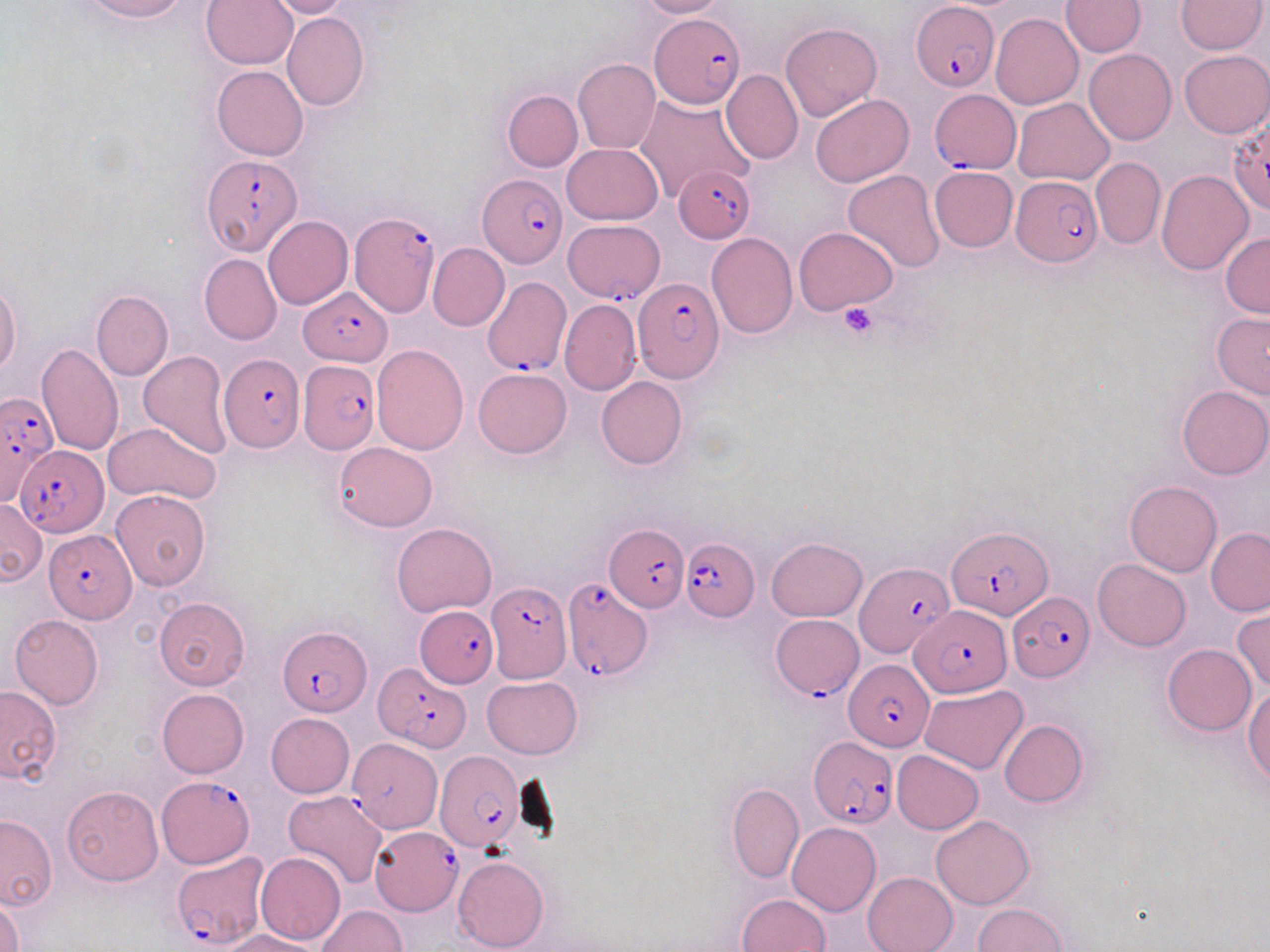
Approximate bounding boxes as (x1, y1, x2, y2) in pixels. Platelet locations: (838, 302, 880, 341). Plasmodium falciparum-infected red blood cell locations: (912, 3, 999, 92), (651, 13, 743, 108), (929, 89, 1021, 172), (1229, 125, 1270, 221), (201, 154, 301, 255), (670, 166, 754, 243), (477, 172, 567, 269), (1012, 174, 1102, 267), (350, 212, 440, 318), (575, 222, 673, 305), (482, 275, 569, 380), (633, 277, 724, 383), (299, 287, 392, 366), (219, 354, 305, 452), (299, 360, 382, 453), (0, 391, 58, 505), (17, 447, 106, 534), (607, 522, 688, 610), (949, 525, 1050, 618), (44, 532, 135, 623), (682, 538, 759, 621), (855, 562, 952, 658), (563, 578, 655, 682), (486, 580, 570, 683), (1010, 591, 1094, 683), (416, 605, 499, 688), (911, 605, 1010, 696), (771, 612, 862, 698), (277, 626, 371, 716), (843, 659, 934, 750), (375, 662, 469, 751), (809, 737, 898, 829), (348, 738, 442, 834), (434, 751, 524, 853), (159, 775, 254, 869), (370, 826, 463, 914), (171, 852, 269, 950). Uninfected red blood cell locations: (79, 0, 188, 22), (637, 0, 727, 19), (1060, 0, 1146, 57), (201, 1, 298, 70), (265, 1, 352, 19), (1174, 1, 1267, 54), (281, 11, 368, 111), (990, 13, 1083, 109), (781, 22, 883, 122), (1084, 49, 1176, 144), (1179, 49, 1270, 136), (572, 59, 660, 154), (212, 65, 307, 160), (721, 68, 803, 164), (503, 90, 583, 171), (634, 93, 755, 202), (810, 94, 915, 186), (1014, 97, 1115, 185), (561, 143, 663, 225), (1090, 156, 1165, 250), (929, 166, 1018, 251), (1155, 169, 1254, 275), (843, 170, 947, 274), (263, 216, 352, 310), (794, 227, 897, 313), (706, 232, 798, 340), (1220, 233, 1270, 319), (427, 243, 509, 332), (199, 254, 282, 345), (0, 282, 22, 377), (91, 289, 173, 381), (559, 300, 640, 395), (1211, 312, 1270, 400), (36, 343, 124, 455), (370, 344, 469, 455), (139, 350, 233, 458), (474, 367, 572, 458), (596, 376, 686, 470), (1178, 385, 1270, 479), (102, 423, 221, 504), (333, 441, 437, 532), (1124, 480, 1222, 576), (110, 489, 210, 589), (0, 499, 47, 588), (391, 522, 497, 615), (1205, 529, 1269, 615), (767, 538, 866, 622), (1093, 560, 1191, 651), (154, 597, 250, 690), (1232, 609, 1270, 694), (10, 615, 104, 709), (1163, 644, 1255, 736), (484, 676, 581, 759), (1243, 685, 1270, 785), (0, 686, 62, 784), (921, 686, 1027, 773), (157, 688, 249, 778), (265, 713, 355, 798), (999, 720, 1087, 807), (893, 751, 983, 834), (727, 782, 804, 884), (61, 786, 164, 885), (283, 790, 389, 889), (930, 815, 1035, 908), (0, 816, 57, 911), (787, 822, 881, 916), (255, 852, 346, 946), (454, 855, 549, 952), (862, 872, 957, 952), (737, 894, 831, 952), (1, 895, 24, 952), (971, 902, 1069, 951), (316, 905, 406, 952), (221, 930, 325, 951). Slide-level diagnosis: Plasmodium falciparum. Captured at 1000x magnification. Image is 1270×952 pixels. One field of a larger specimen. Light microscopy. Thin blood film. May-Grünwald-Giemsa stain.